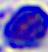

magnification: 400x
identification: white blood cell
modality: micrograph